Comment on the morphology of the erythrocytes.
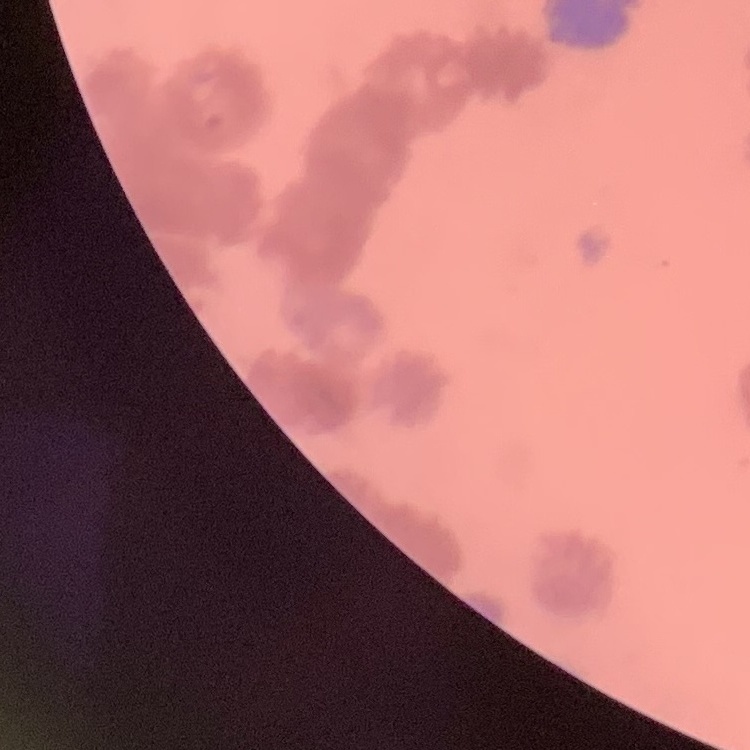
Rouleaux formation.

One tile cut from a larger photomicrograph. Stained with either Field's or Giemsa. Thin blood film.